Find each parasitized red blood cell.
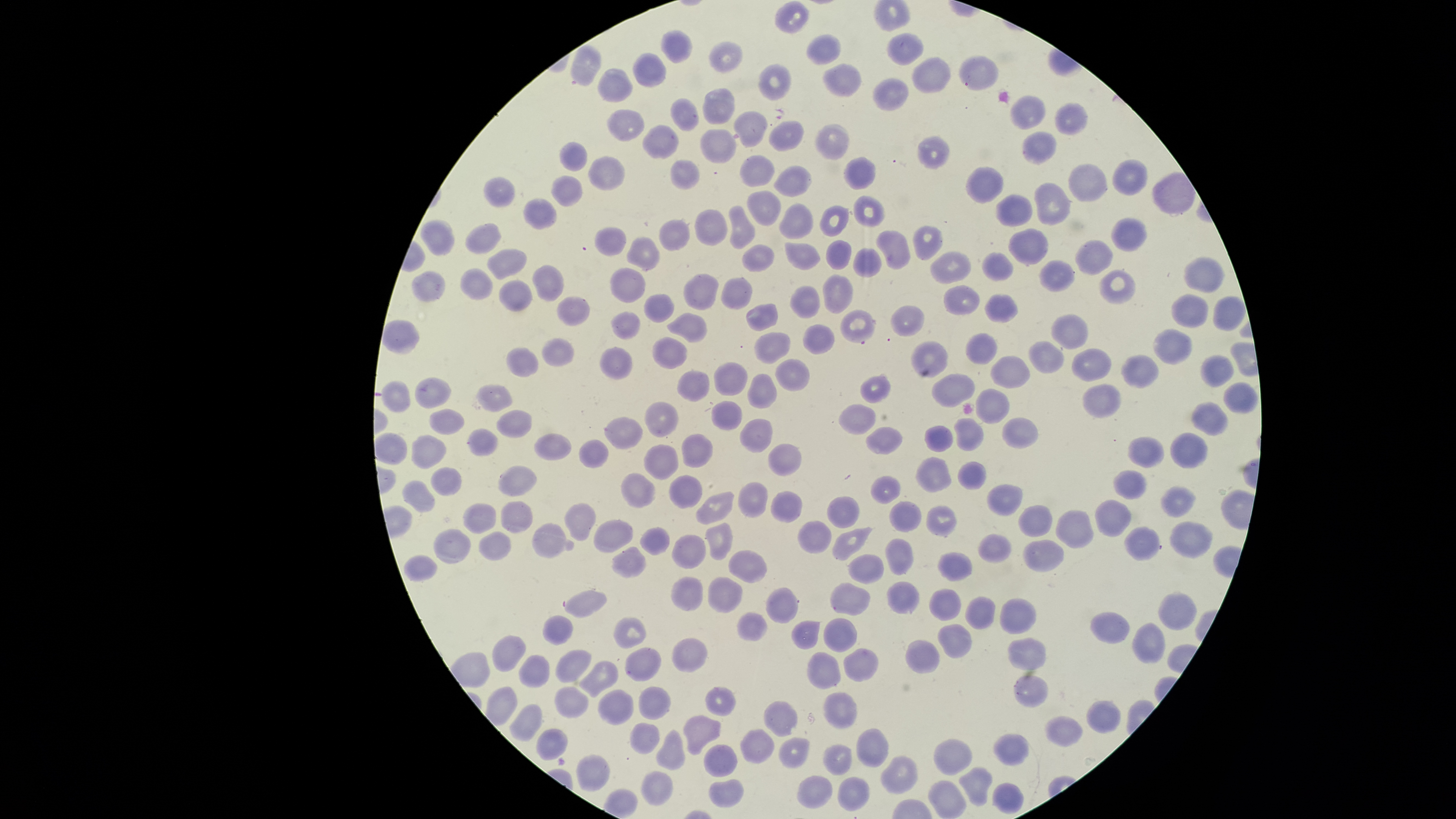

No parasitized red blood cells identified.

Approximate bounding boxes as (left, top, right, bottom) in pixels. Uninfected red blood cells: (775, 1, 807, 35), (660, 30, 693, 64), (886, 31, 923, 66), (807, 33, 841, 66), (709, 41, 743, 74), (570, 44, 601, 85), (632, 53, 666, 87), (959, 53, 998, 92), (913, 57, 952, 93), (759, 63, 791, 102), (822, 63, 861, 96), (597, 68, 632, 104), (872, 77, 909, 111), (701, 89, 733, 125), (1009, 94, 1045, 131), (669, 98, 699, 131), (1055, 101, 1087, 135), (606, 109, 644, 141), (733, 111, 768, 148), (769, 121, 804, 151), (814, 123, 849, 161), (643, 124, 679, 159), (701, 129, 735, 164), (1022, 131, 1056, 166), (917, 135, 949, 169), (560, 141, 587, 173), (588, 155, 623, 192), (738, 155, 776, 188), (844, 156, 876, 190), (670, 159, 701, 190), (1112, 159, 1148, 195), (1067, 163, 1108, 202), (773, 166, 813, 198), (965, 167, 1003, 204), (484, 176, 515, 208), (551, 176, 581, 207), (1035, 182, 1071, 225), (746, 189, 781, 226), (996, 194, 1032, 226), (853, 196, 886, 228), (524, 197, 557, 230), (779, 203, 813, 239), (819, 205, 850, 237), (730, 206, 756, 250), (694, 209, 729, 246), (1111, 215, 1148, 252), (420, 218, 454, 256), (658, 218, 690, 251), (466, 222, 501, 255), (913, 226, 944, 261), (594, 227, 628, 256), (1009, 227, 1049, 265), (875, 229, 911, 271), (626, 237, 659, 271), (1074, 239, 1112, 275), (826, 240, 851, 270), (784, 242, 820, 271), (742, 244, 776, 272), (854, 247, 881, 278), (487, 248, 528, 280), (930, 250, 972, 284), (981, 252, 1015, 282), (1183, 256, 1224, 293), (1039, 260, 1075, 292), (530, 264, 565, 301), (611, 267, 645, 305), (460, 268, 492, 301), (1098, 268, 1137, 305), (412, 271, 444, 303), (822, 273, 853, 315), (683, 274, 720, 310), (721, 278, 754, 310), (498, 280, 533, 312), (943, 284, 979, 315), (789, 285, 820, 319), (1170, 292, 1209, 328), (644, 293, 674, 323), (984, 294, 1018, 324), (556, 296, 591, 326), (1213, 296, 1244, 331), (745, 303, 779, 332), (890, 305, 925, 337), (840, 309, 876, 342), (612, 310, 641, 340), (1050, 313, 1087, 349), (667, 314, 707, 343), (803, 324, 835, 355), (1151, 328, 1191, 366), (965, 331, 998, 364), (754, 332, 791, 364), (653, 335, 687, 370), (542, 338, 574, 367), (911, 339, 948, 379), (1028, 340, 1064, 373), (506, 347, 539, 378), (600, 347, 633, 381), (1071, 348, 1112, 381), (1199, 353, 1234, 388), (1122, 354, 1160, 388), (990, 356, 1031, 389), (775, 359, 810, 392), (713, 361, 749, 396), (677, 370, 709, 403), (747, 373, 777, 408), (931, 374, 975, 407), (861, 376, 891, 404), (415, 378, 452, 409), (381, 381, 412, 412), (1223, 382, 1258, 413), (476, 383, 512, 413), (1084, 384, 1121, 418), (976, 388, 1009, 425), (643, 401, 679, 438), (711, 401, 742, 431), (1193, 402, 1228, 436), (839, 403, 875, 436), (429, 408, 465, 436), (495, 409, 531, 439), (605, 416, 643, 449), (1002, 417, 1039, 449), (739, 418, 774, 453), (952, 419, 982, 451), (866, 425, 904, 455), (925, 425, 956, 453), (467, 428, 498, 456), (534, 433, 571, 462), (1172, 433, 1208, 468), (412, 435, 447, 470), (682, 435, 713, 468), (1127, 438, 1166, 468), (578, 439, 609, 469), (643, 444, 679, 480), (768, 444, 801, 476), (915, 457, 953, 493), (957, 460, 987, 490), (498, 466, 536, 497), (429, 467, 462, 497), (1112, 470, 1147, 499), (621, 473, 654, 508), (669, 475, 703, 509), (871, 475, 902, 505), (401, 480, 435, 513), (738, 482, 768, 518), (987, 484, 1023, 516), (1161, 487, 1195, 518), (770, 490, 803, 523), (695, 492, 735, 525), (826, 496, 861, 528), (501, 500, 533, 535), (1095, 500, 1133, 537), (462, 502, 496, 534), (889, 502, 922, 532), (565, 503, 595, 541), (926, 506, 959, 537), (1019, 506, 1053, 537), (1055, 511, 1094, 548), (594, 520, 634, 553), (706, 520, 733, 562), (797, 521, 832, 554), (1170, 521, 1214, 559), (532, 523, 567, 559), (639, 526, 670, 556), (433, 527, 471, 565), (1125, 527, 1160, 562), (832, 528, 871, 562), (480, 531, 512, 562), (671, 534, 707, 569), (977, 534, 1011, 563), (886, 538, 914, 575), (1022, 539, 1064, 572), (612, 546, 646, 579), (730, 549, 767, 584), (937, 552, 973, 581), (404, 554, 438, 581), (848, 554, 884, 586), (670, 575, 703, 611), (708, 576, 743, 613), (886, 580, 918, 616), (830, 583, 871, 616), (928, 586, 961, 621), (767, 587, 798, 623), (565, 590, 607, 619), (1158, 592, 1196, 632), (964, 595, 995, 630), (999, 598, 1037, 634), (736, 611, 767, 641), (1089, 611, 1130, 643), (541, 615, 572, 646), (613, 616, 645, 649), (824, 618, 858, 652), (792, 620, 819, 649), (1131, 621, 1165, 663), (937, 622, 972, 659), (492, 634, 525, 673), (671, 637, 707, 673), (1008, 637, 1047, 670), (904, 639, 939, 674), (625, 647, 661, 682), (843, 647, 877, 682), (556, 648, 591, 684), (805, 651, 839, 690), (518, 653, 550, 688), (578, 660, 618, 698), (1013, 674, 1048, 709), (554, 685, 588, 720), (638, 685, 671, 720), (704, 686, 737, 717), (597, 688, 633, 726), (823, 691, 857, 729), (764, 700, 798, 737), (1086, 700, 1121, 734), (509, 704, 542, 741), (683, 716, 721, 755), (1044, 716, 1083, 748), (629, 721, 660, 754), (536, 727, 569, 761), (741, 728, 775, 763), (855, 728, 889, 768), (656, 729, 685, 770), (994, 735, 1029, 766), (778, 737, 810, 769), (933, 739, 972, 775), (703, 743, 738, 777), (823, 744, 852, 775), (577, 754, 610, 792), (880, 755, 917, 795), (959, 767, 993, 805), (640, 771, 673, 806), (797, 776, 832, 809), (837, 777, 870, 812), (709, 778, 744, 808), (928, 780, 967, 819), (992, 782, 1024, 814). The visible region is circular. One field of view of the specimen. Photographed with a smartphone camera through the microscope eyepiece. Image is 1456×819 pixels. Thin blood film. Giemsa stain.